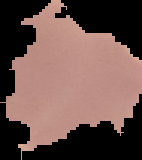

Summary:
  - Preparation: thin blood smear
  - Result: negative for Plasmodium parasites
  - Image size: 142×160 pixels
  - Image type: cell region segmented out of the field of view; surrounding area masked to black